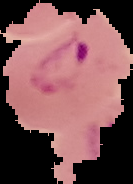
Segmented cell region on a black background. From a thin blood film. Result: Plasmodium parasites detected. Image is 133×184 pixels.